Outline each Plasmodium vivax-infected red blood cell.
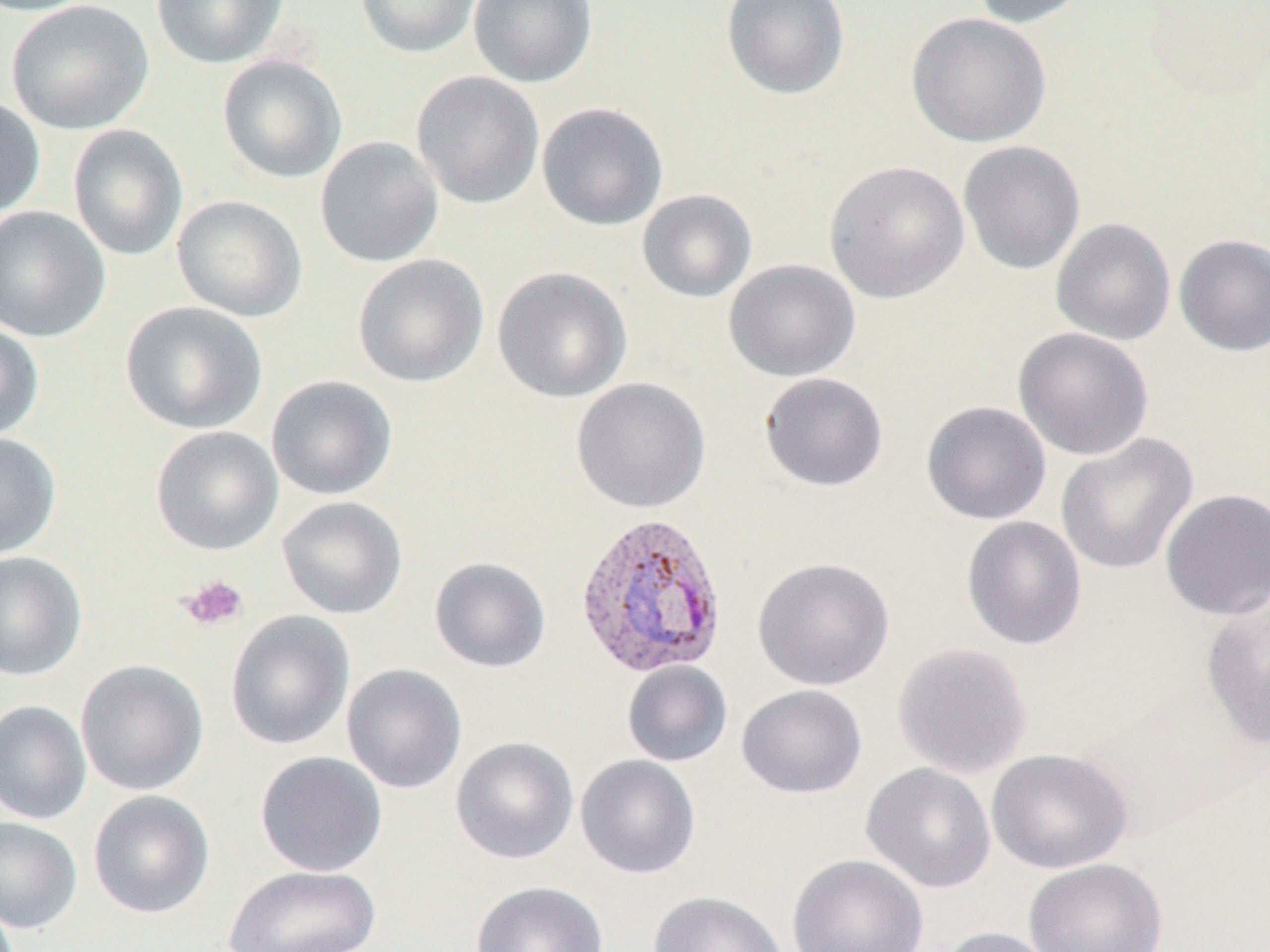
Approximate bounding boxes as named x1/y1/x2/y2 corners in pixels.
Plasmodium vivax-infected red blood cells: (x1=573, y1=511, x2=729, y2=680).

Platelet locations: (x1=178, y1=575, x2=248, y2=631). Uninfected red blood cell locations: (x1=0, y1=0, x2=104, y2=17), (x1=6, y1=0, x2=154, y2=135), (x1=151, y1=0, x2=289, y2=69), (x1=355, y1=0, x2=482, y2=59), (x1=468, y1=0, x2=598, y2=88), (x1=721, y1=0, x2=851, y2=101), (x1=970, y1=0, x2=1092, y2=29), (x1=1139, y1=1, x2=1269, y2=103), (x1=906, y1=12, x2=1052, y2=148), (x1=217, y1=54, x2=347, y2=183), (x1=411, y1=70, x2=545, y2=209), (x1=0, y1=93, x2=46, y2=218), (x1=537, y1=102, x2=669, y2=231), (x1=68, y1=124, x2=188, y2=262), (x1=315, y1=136, x2=444, y2=268), (x1=958, y1=140, x2=1086, y2=276), (x1=824, y1=160, x2=970, y2=303), (x1=637, y1=189, x2=758, y2=303), (x1=172, y1=195, x2=307, y2=322), (x1=0, y1=206, x2=111, y2=343), (x1=1051, y1=218, x2=1176, y2=346), (x1=1174, y1=234, x2=1270, y2=356), (x1=352, y1=254, x2=489, y2=388), (x1=723, y1=258, x2=861, y2=382), (x1=491, y1=266, x2=633, y2=404), (x1=120, y1=301, x2=268, y2=435), (x1=0, y1=321, x2=44, y2=441), (x1=1013, y1=327, x2=1154, y2=461), (x1=759, y1=372, x2=889, y2=492), (x1=266, y1=375, x2=398, y2=500), (x1=571, y1=377, x2=711, y2=514), (x1=922, y1=400, x2=1052, y2=525), (x1=150, y1=426, x2=283, y2=556), (x1=0, y1=431, x2=61, y2=560), (x1=1056, y1=433, x2=1198, y2=575), (x1=1160, y1=488, x2=1270, y2=621), (x1=277, y1=496, x2=408, y2=620), (x1=962, y1=516, x2=1087, y2=650), (x1=0, y1=551, x2=87, y2=681), (x1=429, y1=556, x2=552, y2=673), (x1=753, y1=558, x2=894, y2=690), (x1=1201, y1=598, x2=1270, y2=749), (x1=225, y1=610, x2=356, y2=751), (x1=892, y1=642, x2=1033, y2=779), (x1=75, y1=659, x2=209, y2=796), (x1=622, y1=661, x2=733, y2=767), (x1=342, y1=663, x2=468, y2=794), (x1=736, y1=684, x2=867, y2=799), (x1=0, y1=700, x2=92, y2=825), (x1=450, y1=736, x2=579, y2=865), (x1=986, y1=748, x2=1134, y2=874), (x1=255, y1=751, x2=388, y2=877), (x1=575, y1=754, x2=701, y2=879), (x1=861, y1=763, x2=996, y2=893), (x1=88, y1=790, x2=215, y2=919), (x1=0, y1=816, x2=82, y2=934), (x1=786, y1=854, x2=928, y2=952), (x1=1023, y1=858, x2=1168, y2=952), (x1=225, y1=864, x2=382, y2=952), (x1=469, y1=880, x2=609, y2=952), (x1=647, y1=890, x2=790, y2=952), (x1=937, y1=926, x2=1059, y2=952). Slide-level diagnosis: Plasmodium vivax. 1000x magnification. Image is 1270×952 pixels. May-Grünwald-Giemsa-stained preparation. Thin blood film. Optical microscopy. One field of a larger specimen.